Report the malaria status of this cell.
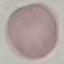

It is uninfected.

Summary:
  - Capture: smartphone through the microscope eyepiece
  - Preparation: thin smear
  - Image type: cell patch, automatically extracted from a larger field of view and resized to 64 × 64 pixels
  - Stain: Giemsa